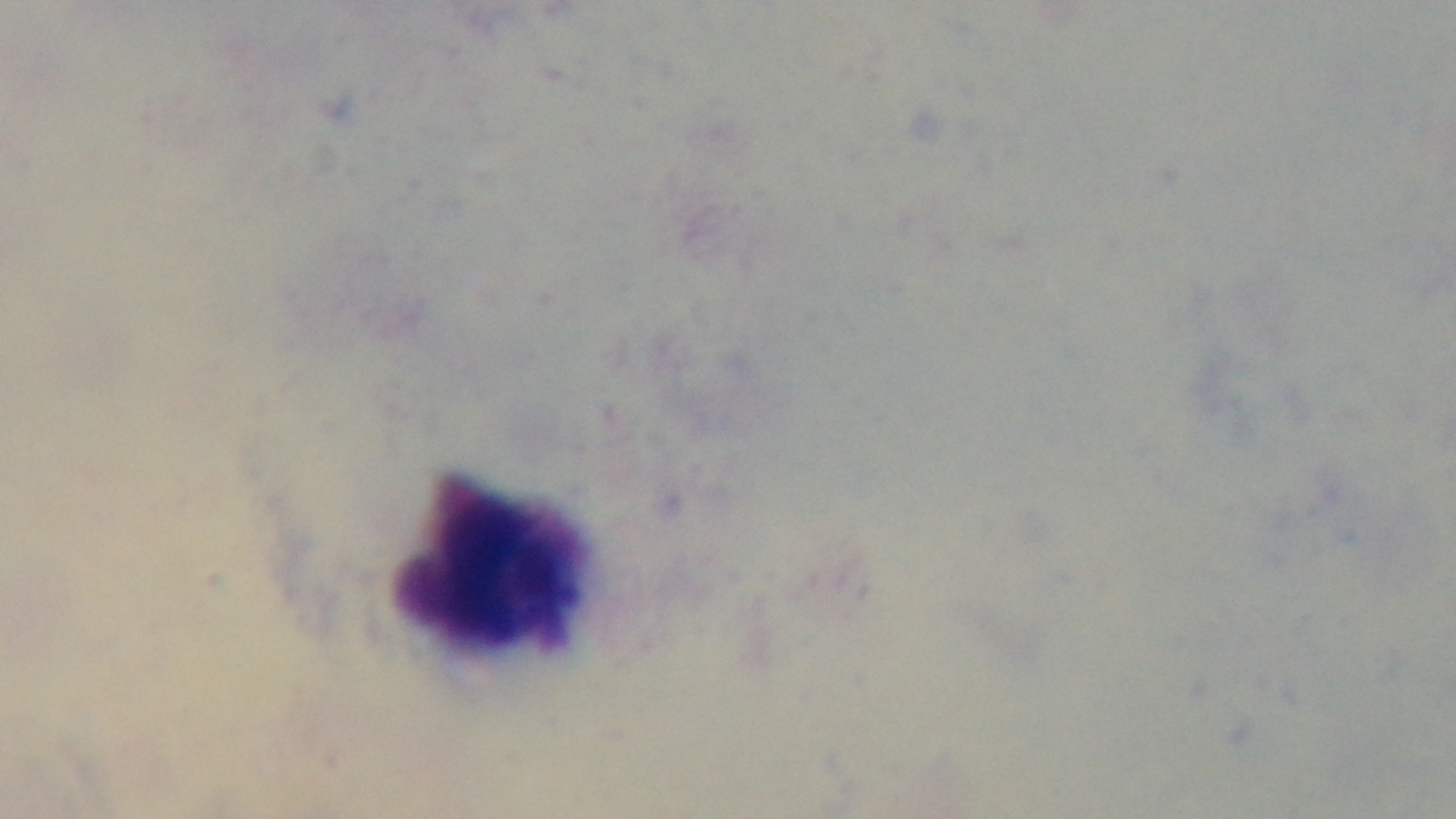

{
  "modality": "light microscopy",
  "objective": "100x oil immersion",
  "malaria_status": "uninfected",
  "preparation": "thick smear",
  "field_of_view": "one from the slide",
  "stain": "Giemsa",
  "capture": "mounted 4K digital camera"
}